Identify the parasite.
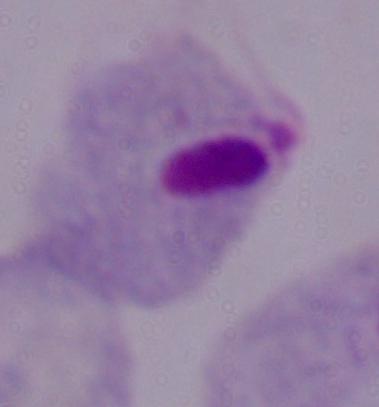

This is a trichomonad.

1000x magnification. Photomicrograph.